Report the malaria status of this cell.
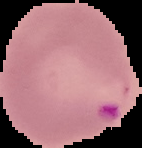
It is parasitized.

From a thin blood film. Image is 142×148 pixels. Segmented cell region on a black background.